Identify the preparation type.
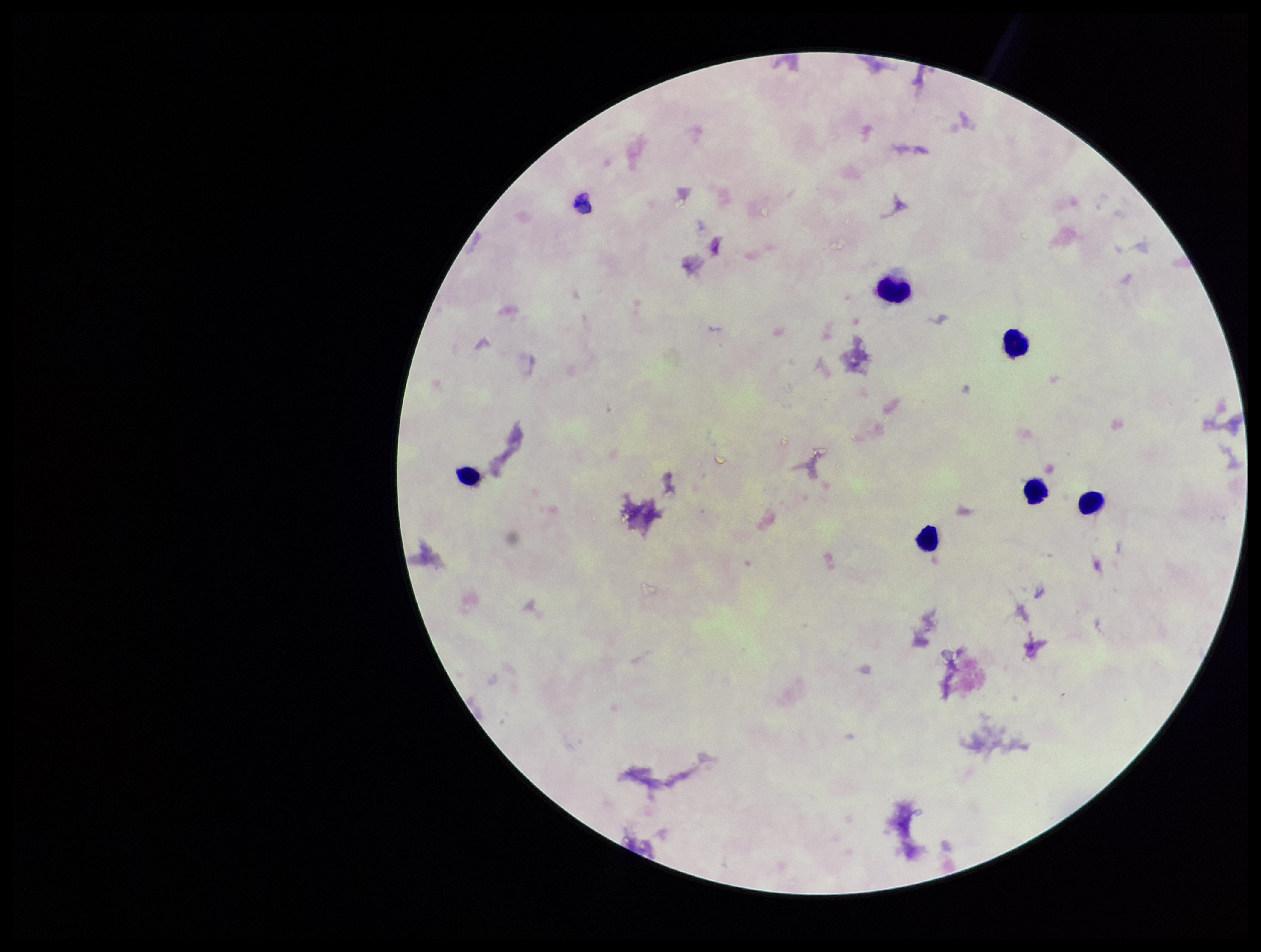
A thick smear.

Summary:
  - Image size: 1261×952 pixels
  - Leukocyte count: 6
  - Field of view: one from this slide
  - Plasmodium parasites: none detected
  - Patient malaria status: negative
  - Parasite count: 0
  - Capture: smartphone photograph through the microscope eyepiece
  - Stain: Giemsa